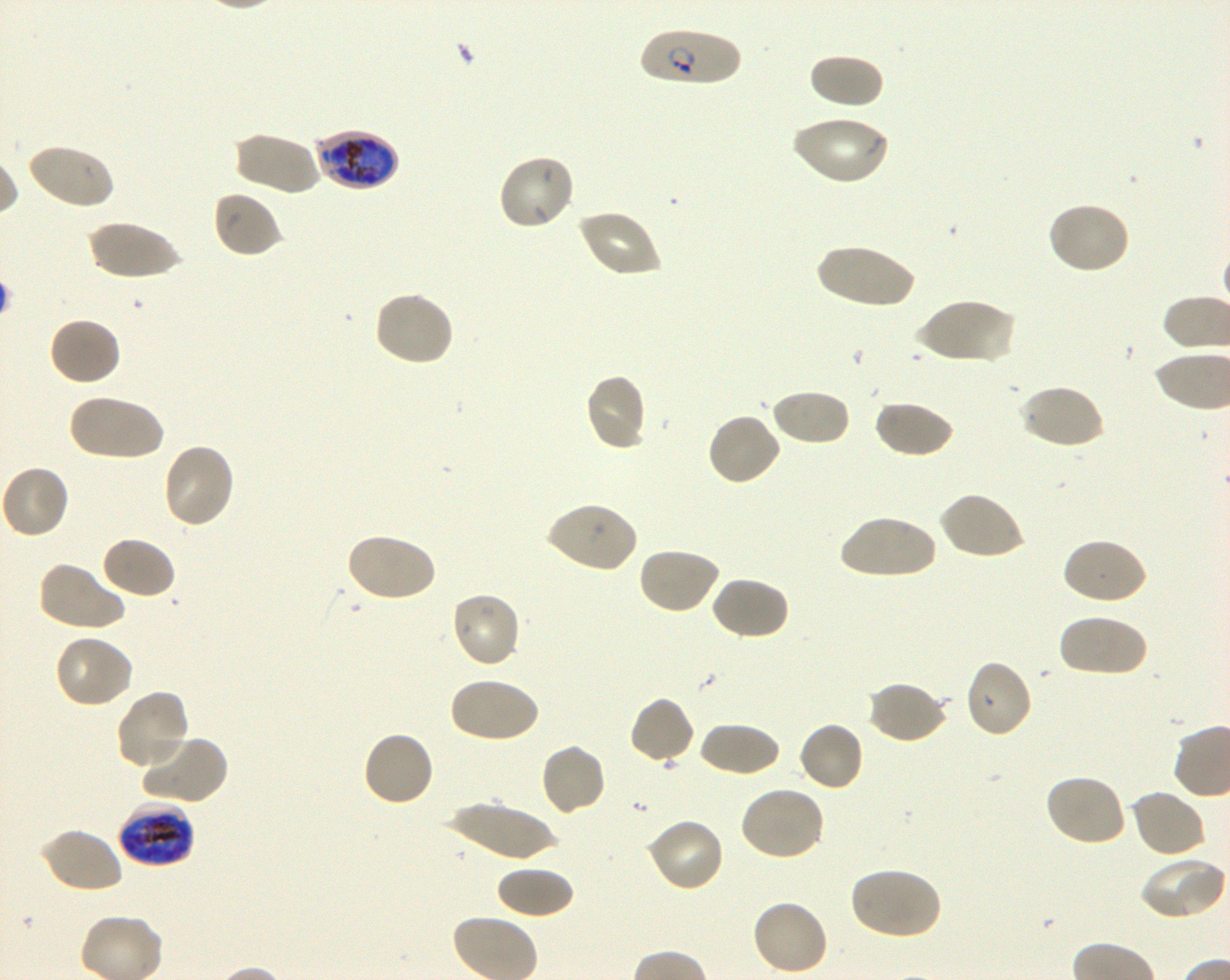

Not every red blood cell is marked. A life-cycle stage — or a range of stages, where the recorded stages span more than one — follows each staged infected red blood cell.
donor_blood_group: O+
objective: 100x, oil immersion, numerical aperture 1.30
locations_of_infected_red_blood_cells: 'approximate bounding rectangles given as corner coordinates in pixels from the top-left: (x1=639, y1=28, x2=742, y2=87) ring; (x1=313, y1=130, x2=400, y2=191) late trophozoite to early schizont; (x1=119, y1=801, x2=194, y2=870) late trophozoite to late schizont'
field_of_view: one from this slide
preparation: thin blood smear
locations_of_uninfected_red_blood_cells: 'approximate bounding rectangles given as corner coordinates in pixels from the top-left: (x1=808, y1=53, x2=884, y2=109), (x1=790, y1=114, x2=889, y2=186), (x1=232, y1=131, x2=321, y2=196), (x1=26, y1=142, x2=116, y2=211), (x1=497, y1=153, x2=576, y2=231), (x1=211, y1=190, x2=282, y2=258), (x1=1047, y1=201, x2=1132, y2=276), (x1=577, y1=208, x2=661, y2=278), (x1=88, y1=221, x2=183, y2=280), (x1=814, y1=244, x2=919, y2=309), (x1=372, y1=290, x2=456, y2=367), (x1=914, y1=297, x2=1015, y2=366), (x1=47, y1=316, x2=122, y2=387), (x1=583, y1=373, x2=648, y2=452), (x1=1018, y1=383, x2=1105, y2=451), (x1=769, y1=389, x2=850, y2=447), (x1=67, y1=392, x2=164, y2=461), (x1=874, y1=400, x2=956, y2=459), (x1=705, y1=412, x2=782, y2=488), (x1=161, y1=442, x2=236, y2=529), (x1=0, y1=464, x2=70, y2=540), (x1=939, y1=490, x2=1026, y2=560), (x1=543, y1=501, x2=637, y2=574), (x1=838, y1=515, x2=938, y2=580), (x1=345, y1=532, x2=438, y2=604), (x1=99, y1=535, x2=177, y2=600), (x1=1061, y1=537, x2=1147, y2=606), (x1=637, y1=546, x2=720, y2=615), (x1=37, y1=560, x2=128, y2=632), (x1=710, y1=575, x2=789, y2=641), (x1=449, y1=591, x2=522, y2=669), (x1=1057, y1=613, x2=1148, y2=678), (x1=53, y1=634, x2=135, y2=709), (x1=963, y1=659, x2=1034, y2=740), (x1=447, y1=677, x2=539, y2=744), (x1=867, y1=680, x2=949, y2=745), (x1=114, y1=689, x2=192, y2=770), (x1=629, y1=695, x2=695, y2=765), (x1=796, y1=720, x2=865, y2=793), (x1=698, y1=721, x2=781, y2=778), (x1=362, y1=730, x2=434, y2=809), (x1=139, y1=733, x2=228, y2=805), (x1=539, y1=742, x2=608, y2=817), (x1=1043, y1=773, x2=1127, y2=847), (x1=737, y1=786, x2=827, y2=862), (x1=1129, y1=789, x2=1207, y2=859), (x1=447, y1=801, x2=559, y2=862), (x1=646, y1=817, x2=726, y2=893), (x1=40, y1=828, x2=123, y2=895), (x1=1139, y1=857, x2=1226, y2=921), (x1=494, y1=864, x2=575, y2=919), (x1=849, y1=866, x2=942, y2=941), (x1=750, y1=898, x2=829, y2=976)'
stain: Giemsa
image_size: 1230×980 pixels
culture: shaking in-vitro Plasmodium falciparum strain 3D7